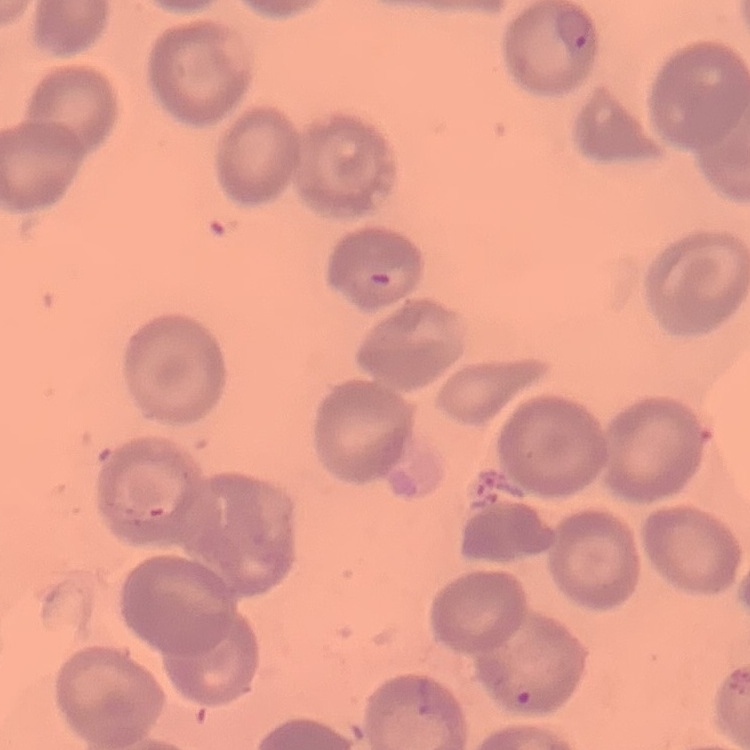
The erythrocytes show no rouleaux formation. One tile cut from a larger photomicrograph. Thin blood film. Stained with either Field's or Giemsa.